Comment on the morphology of the erythrocytes.
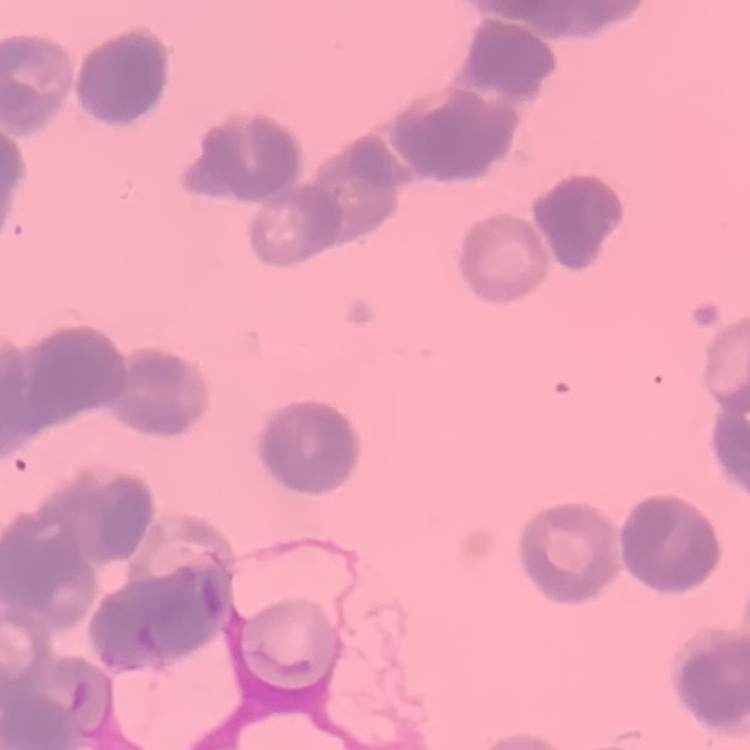

Rouleaux formation.

Stained with either Field's or Giemsa. One tile cut from a larger photomicrograph. Thin blood smear.